State which parasite is depicted.
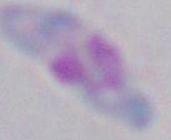
Toxoplasma gondii.

Summary:
  - Magnification: 1000x
  - Modality: photomicrograph